State which parasite is depicted.
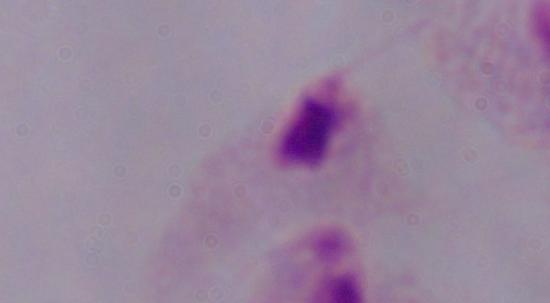

This is a trichomonad.

modality: photomicrograph
magnification: 1000x